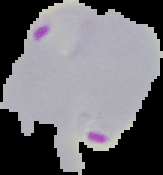
Segmented cell region on a black background. Malaria status: parasitized. Image is 163×175 pixels. From a thin blood smear.